State the blood parasite species.
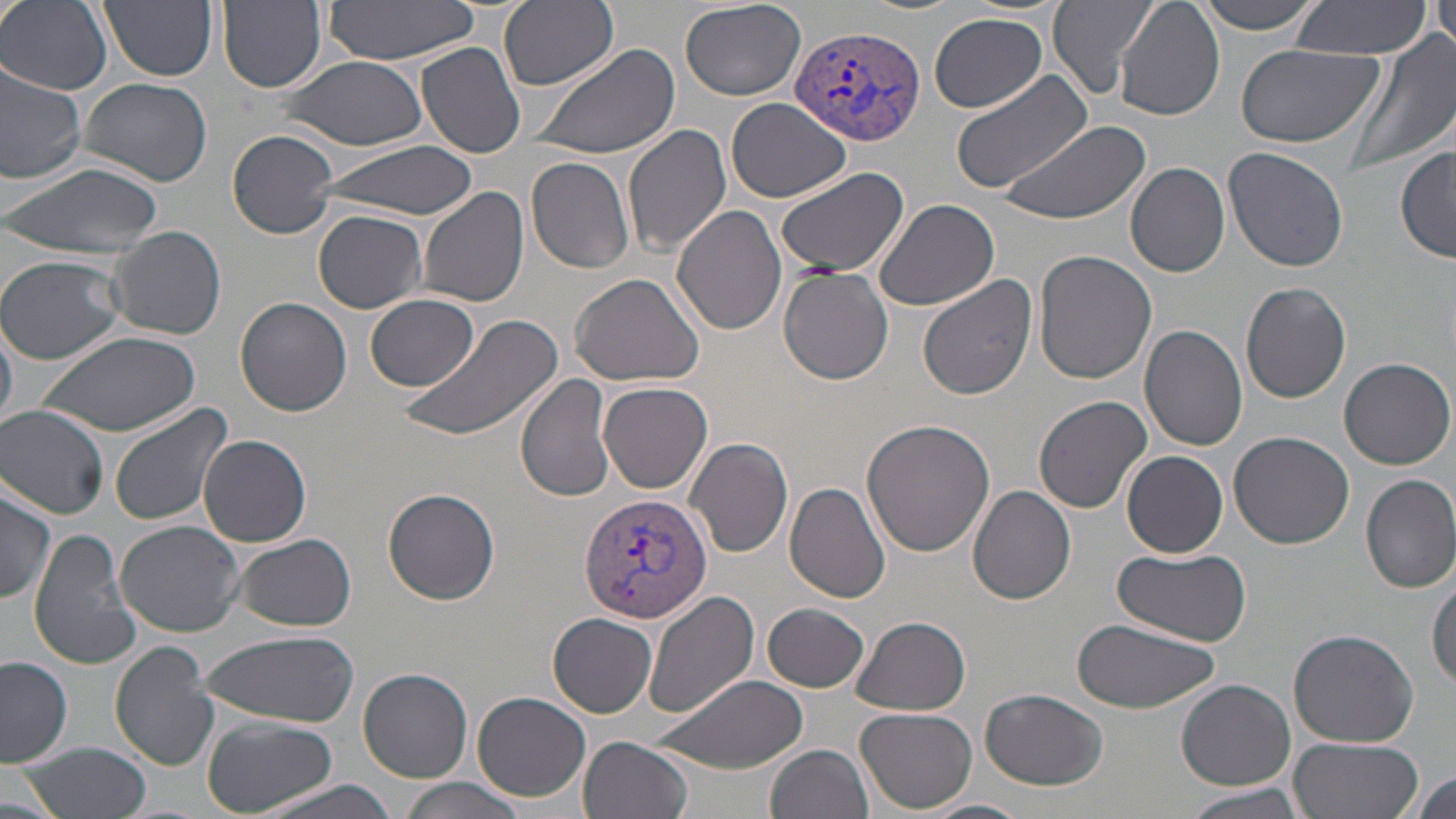
Plasmodium vivax.

Approximate bounding boxes as named x1/y1/x2/y2 corners in pixels. Uninfected red blood cell locations: (x1=1, y1=0, x2=113, y2=95), (x1=100, y1=0, x2=218, y2=81), (x1=218, y1=0, x2=327, y2=92), (x1=500, y1=0, x2=619, y2=91), (x1=677, y1=0, x2=807, y2=101), (x1=1049, y1=0, x2=1161, y2=99), (x1=1115, y1=0, x2=1225, y2=121), (x1=1195, y1=0, x2=1323, y2=34), (x1=1290, y1=0, x2=1431, y2=57), (x1=323, y1=1, x2=484, y2=64), (x1=1430, y1=4, x2=1456, y2=49), (x1=928, y1=13, x2=1048, y2=113), (x1=1344, y1=28, x2=1452, y2=177), (x1=416, y1=41, x2=527, y2=159), (x1=534, y1=42, x2=682, y2=162), (x1=1234, y1=43, x2=1385, y2=149), (x1=277, y1=54, x2=430, y2=151), (x1=0, y1=62, x2=88, y2=184), (x1=951, y1=70, x2=1092, y2=194), (x1=77, y1=76, x2=213, y2=186), (x1=726, y1=97, x2=851, y2=203), (x1=998, y1=119, x2=1152, y2=227), (x1=624, y1=124, x2=734, y2=257), (x1=228, y1=130, x2=338, y2=237), (x1=312, y1=142, x2=479, y2=219), (x1=1395, y1=144, x2=1455, y2=262), (x1=1222, y1=147, x2=1350, y2=274), (x1=525, y1=156, x2=635, y2=275), (x1=2, y1=160, x2=165, y2=263), (x1=1125, y1=162, x2=1231, y2=278), (x1=774, y1=167, x2=909, y2=279), (x1=417, y1=186, x2=530, y2=309), (x1=875, y1=198, x2=1000, y2=312), (x1=672, y1=204, x2=788, y2=336), (x1=313, y1=209, x2=428, y2=312), (x1=107, y1=226, x2=226, y2=340), (x1=1033, y1=249, x2=1157, y2=384), (x1=0, y1=254, x2=126, y2=367), (x1=777, y1=267, x2=894, y2=385), (x1=569, y1=272, x2=706, y2=387), (x1=917, y1=277, x2=1034, y2=402), (x1=1240, y1=282, x2=1352, y2=404), (x1=365, y1=293, x2=481, y2=391), (x1=236, y1=297, x2=353, y2=417), (x1=397, y1=313, x2=564, y2=441), (x1=1, y1=322, x2=16, y2=432), (x1=1140, y1=322, x2=1250, y2=451), (x1=38, y1=330, x2=199, y2=435), (x1=1339, y1=358, x2=1454, y2=469), (x1=517, y1=374, x2=618, y2=502), (x1=599, y1=382, x2=712, y2=494), (x1=1033, y1=395, x2=1153, y2=514), (x1=109, y1=402, x2=237, y2=530), (x1=1, y1=406, x2=110, y2=519), (x1=861, y1=420, x2=994, y2=558), (x1=1228, y1=430, x2=1355, y2=549), (x1=198, y1=434, x2=312, y2=548), (x1=684, y1=435, x2=793, y2=559), (x1=1123, y1=451, x2=1228, y2=559), (x1=1360, y1=472, x2=1456, y2=593), (x1=785, y1=481, x2=894, y2=604), (x1=0, y1=486, x2=56, y2=606), (x1=968, y1=486, x2=1078, y2=605), (x1=383, y1=487, x2=500, y2=604), (x1=115, y1=520, x2=245, y2=638), (x1=29, y1=530, x2=140, y2=671), (x1=228, y1=532, x2=357, y2=632), (x1=1112, y1=548, x2=1251, y2=645), (x1=1430, y1=572, x2=1456, y2=694), (x1=645, y1=589, x2=761, y2=720), (x1=762, y1=603, x2=870, y2=693), (x1=548, y1=614, x2=658, y2=717), (x1=848, y1=615, x2=973, y2=712), (x1=1071, y1=617, x2=1223, y2=712), (x1=1288, y1=629, x2=1420, y2=748), (x1=199, y1=631, x2=359, y2=727), (x1=109, y1=642, x2=218, y2=771), (x1=1, y1=655, x2=73, y2=766), (x1=357, y1=666, x2=473, y2=784), (x1=645, y1=673, x2=807, y2=774), (x1=1176, y1=679, x2=1295, y2=790), (x1=979, y1=689, x2=1112, y2=790), (x1=473, y1=691, x2=592, y2=801), (x1=855, y1=707, x2=981, y2=814), (x1=201, y1=716, x2=337, y2=815), (x1=578, y1=735, x2=693, y2=819), (x1=1286, y1=737, x2=1429, y2=819), (x1=16, y1=742, x2=153, y2=819), (x1=768, y1=744, x2=875, y2=819), (x1=1407, y1=768, x2=1456, y2=816), (x1=395, y1=777, x2=533, y2=819), (x1=252, y1=780, x2=405, y2=819), (x1=1180, y1=783, x2=1312, y2=819), (x1=918, y1=798, x2=1033, y2=819). Plasmodium vivax-infected red blood cell locations: (x1=792, y1=22, x2=929, y2=147), (x1=579, y1=490, x2=712, y2=624). Image is 1456×819 pixels. Light microscopy. May-Grünwald-Giemsa stain. Single field of view. 1000x magnification. Thin blood smear.